Give a bounding box for every leukocyte visible.
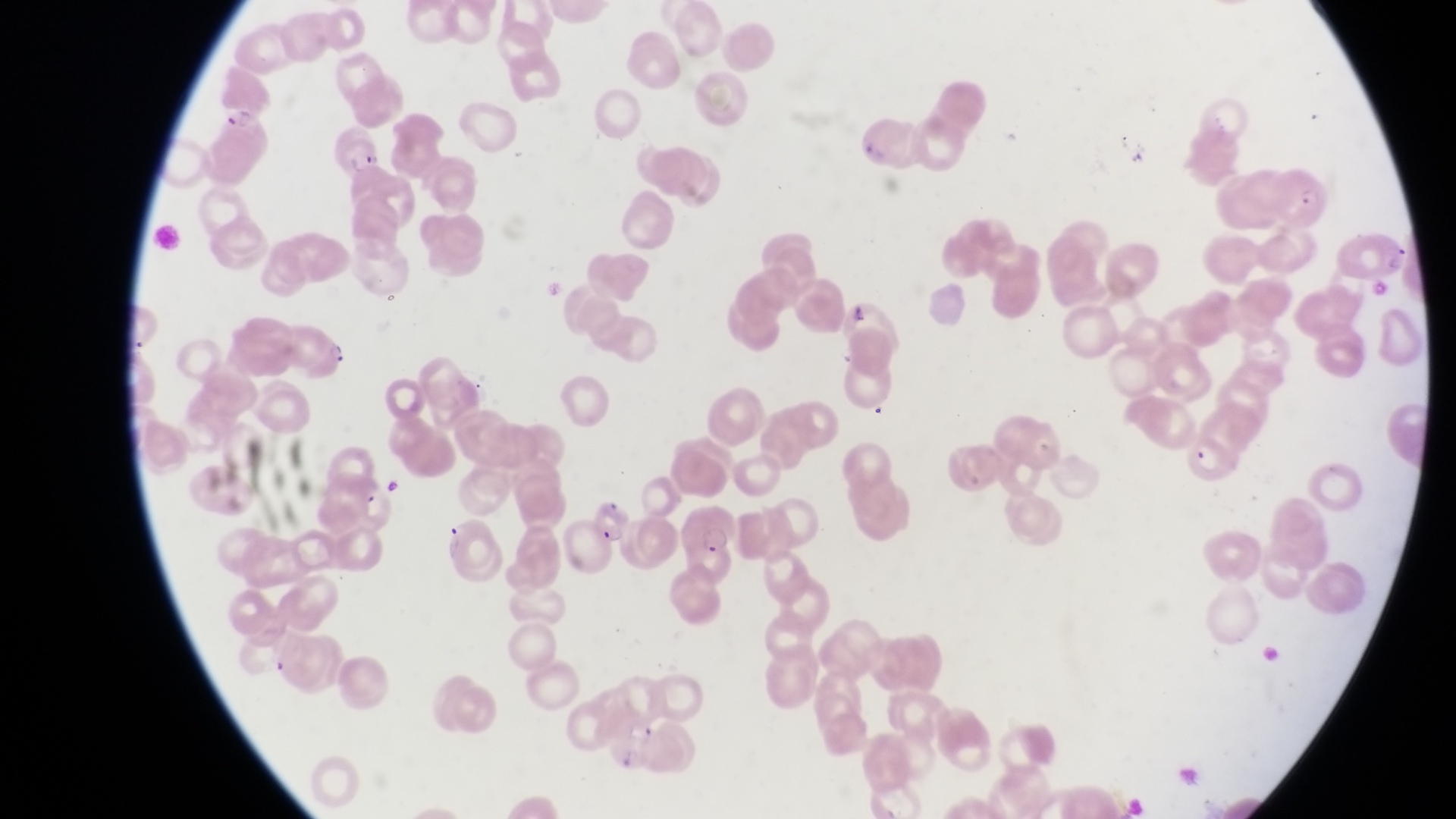

No leukocytes observed.

Approximate bounding boxes as (left, top, right, bottom) in pixels.
Summary:
  - Parasitised red blood cell locations: (208, 106, 271, 165), (333, 135, 391, 181), (1272, 165, 1333, 228), (287, 327, 353, 386), (1181, 425, 1239, 484), (579, 489, 628, 545), (679, 505, 748, 563)
  - Field of view: single
  - Image size: 1456×819 pixels
  - Capture: smartphone photograph through the eyepiece of an Olympus CX-23 microscope
  - Country: Uganda
  - Magnification: 1000x
  - Preparation: thin blood film